Outline each blood parasite and name the species.
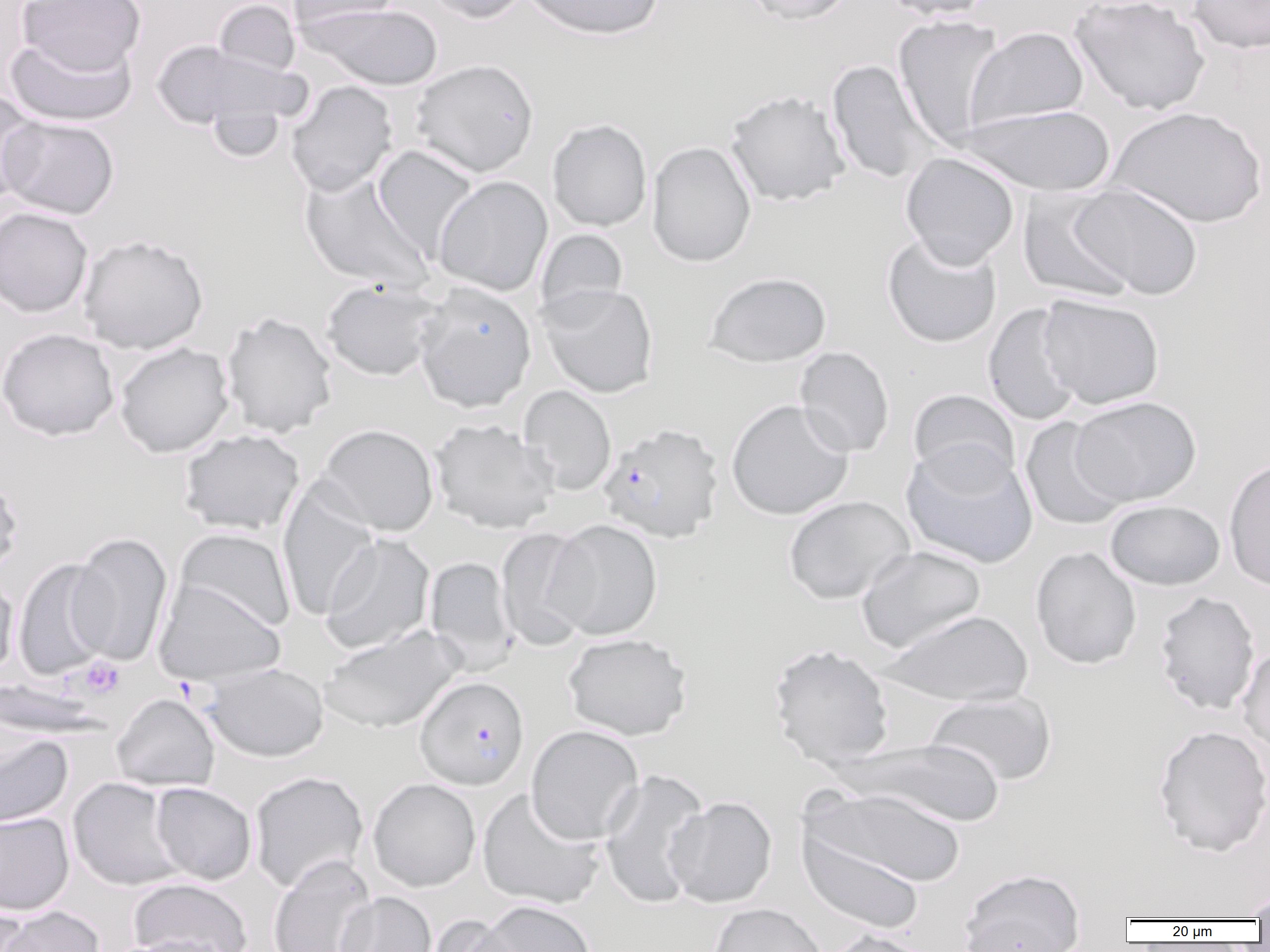
Approximate bounding boxes as (x1,y1)-(x2,y2) corner pairs in pixels.
Plasmodium falciparum-infected red blood cells: (597,423)-(724,544), (415,676)-(529,790).
No Plasmodium ovale, Plasmodium malariae, Plasmodium vivax, Babesia divergens, or Trypanosoma brucei observed.

Summary:
  - Platelet locations: (78,656)-(126,699)
  - Uninfected red blood cell locations: (212,0)-(301,78), (287,0)-(401,34), (423,0)-(532,24), (521,0)-(665,41), (741,0)-(857,26), (879,0)-(994,21), (1069,0)-(1211,115), (1187,0)-(1270,54), (18,1)-(147,76), (300,3)-(444,91), (892,14)-(1005,147), (965,26)-(1089,132), (4,33)-(139,127), (152,39)-(305,140), (409,58)-(539,178), (826,60)-(938,184), (285,80)-(399,196), (724,89)-(851,207), (0,91)-(44,208), (956,104)-(1117,196), (1107,106)-(1268,228), (1,115)-(119,219), (546,119)-(652,232), (646,141)-(756,267), (371,146)-(478,261), (899,152)-(1020,269), (299,170)-(433,292), (433,176)-(553,296), (1069,183)-(1202,300), (1018,188)-(1137,304), (0,206)-(93,319), (534,228)-(629,322), (881,233)-(1002,348), (77,234)-(209,354), (704,271)-(832,367), (320,278)-(446,382), (412,282)-(537,412), (537,283)-(659,398), (1037,293)-(1165,409), (982,303)-(1084,426), (220,311)-(338,438), (0,328)-(120,441), (113,342)-(234,457), (794,346)-(895,458), (518,385)-(617,496), (907,389)-(1021,488), (1070,396)-(1202,506), (725,399)-(854,520), (429,418)-(559,534), (1020,418)-(1130,531), (316,423)-(439,537), (178,428)-(306,536), (900,441)-(1038,568), (1223,457)-(1270,592), (0,470)-(24,579), (277,484)-(380,621), (783,495)-(915,605), (1104,499)-(1225,590), (544,519)-(664,641), (494,526)-(598,651), (173,528)-(296,634), (68,532)-(173,666), (318,533)-(435,655), (855,545)-(987,653), (1030,546)-(1142,669), (424,556)-(519,671), (12,557)-(115,680), (0,574)-(19,681), (154,578)-(286,685), (1153,591)-(1261,715), (880,609)-(1033,707), (318,626)-(463,733), (562,632)-(692,741), (767,643)-(895,769), (1237,644)-(1270,759), (202,662)-(329,762), (923,691)-(1058,787), (111,693)-(221,791), (1152,724)-(1270,857), (525,725)-(645,844), (0,733)-(74,829), (839,739)-(1006,827), (598,768)-(710,909), (249,771)-(369,892), (67,777)-(184,891), (367,778)-(481,892), (151,782)-(257,885), (807,786)-(967,889), (477,787)-(607,910), (664,796)-(778,908), (0,812)-(74,915), (798,830)-(924,935), (268,854)-(376,952), (958,868)-(1087,952), (127,877)-(253,952), (1243,889)-(1270,922), (335,892)-(437,952), (475,900)-(597,952), (0,903)-(34,951), (708,903)-(827,952), (2,905)-(105,952), (423,914)-(525,952), (822,928)-(937,952), (107,935)-(230,952)
  - Slide-level diagnosis: Plasmodium falciparum
  - Magnification: 1000x
  - Preparation: thin blood film
  - Field of view: one of a larger specimen
  - Modality: light microscopy
  - Image size: 1270×952 pixels